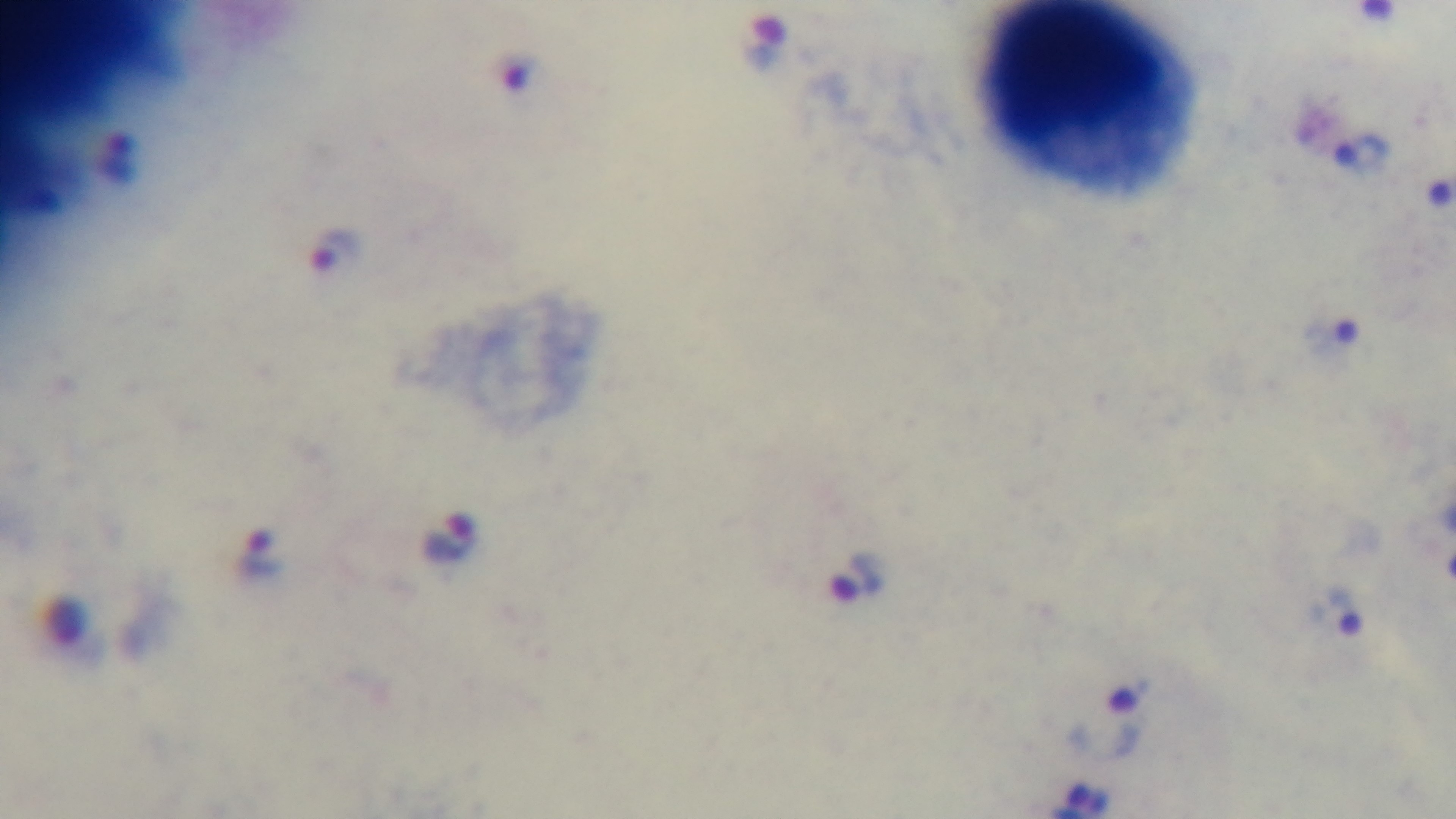 100x oil-immersion objective. Malaria status: positive. Captured with a mounted 4K digital camera. Giemsa-stained. Preparation: thick. Photomicrograph. One field from the slide.